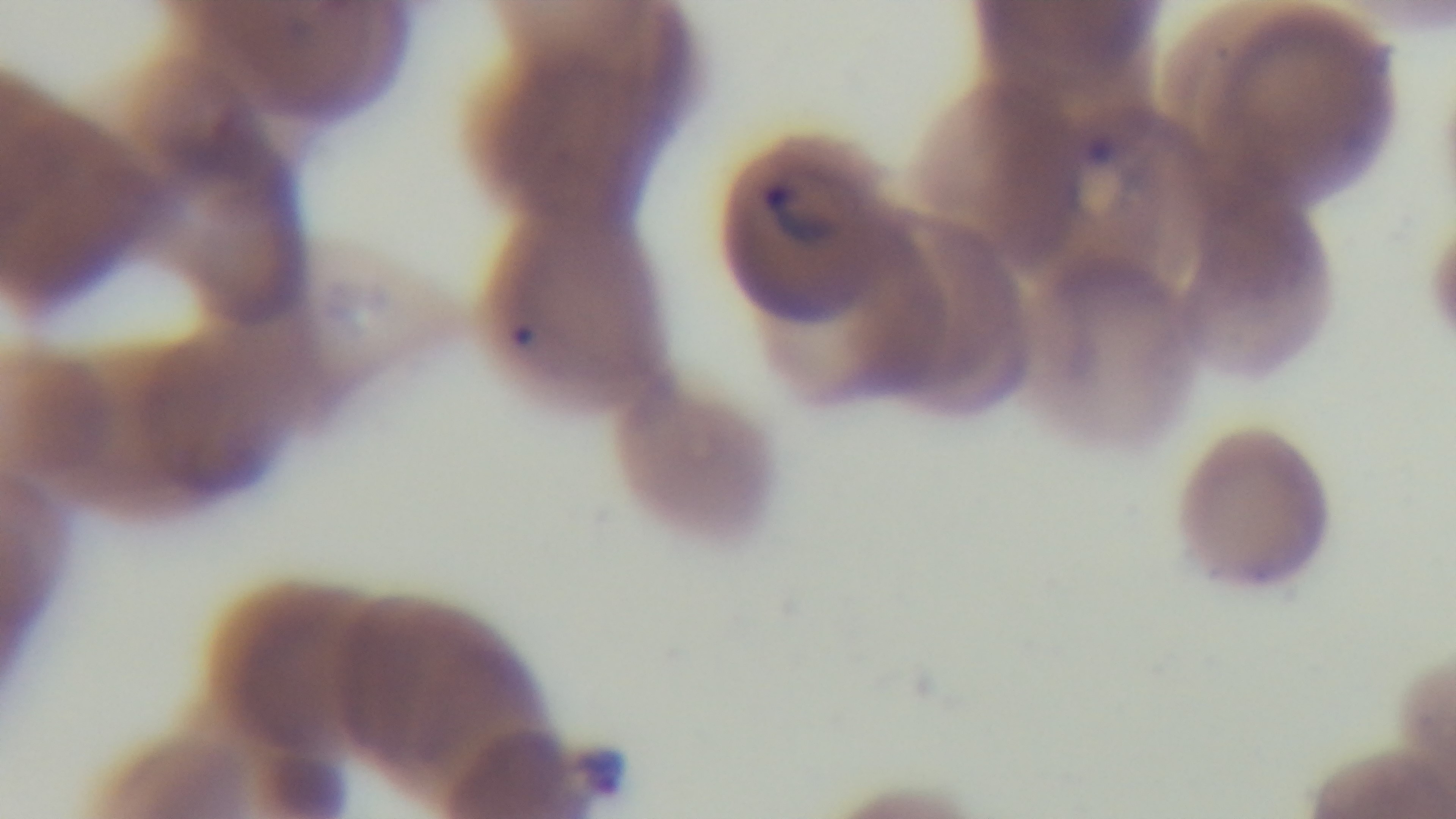

Summary:
  - Modality: light microscopy
  - Malaria status: positive
  - Objective: 100x oil immersion
  - Capture: mounted 4K digital camera
  - Field of view: single
  - Preparation: thin blood film
  - Stain: Giemsa